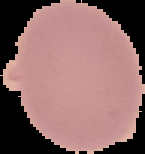
Image is 145×154 pixels. Segmented cell region on a black background. From a thin blood smear. Malaria status: uninfected.